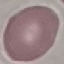

malaria status = uninfected
capture = smartphone through the microscope eyepiece
image type = automatically extracted cell patch, resized to 64 × 64 pixels
stain = Giemsa
preparation = thin smear